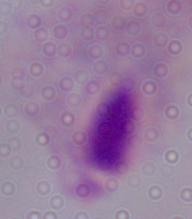
modality = photomicrograph
identification = trichomonad
magnification = 1000x